State the blood parasite species.
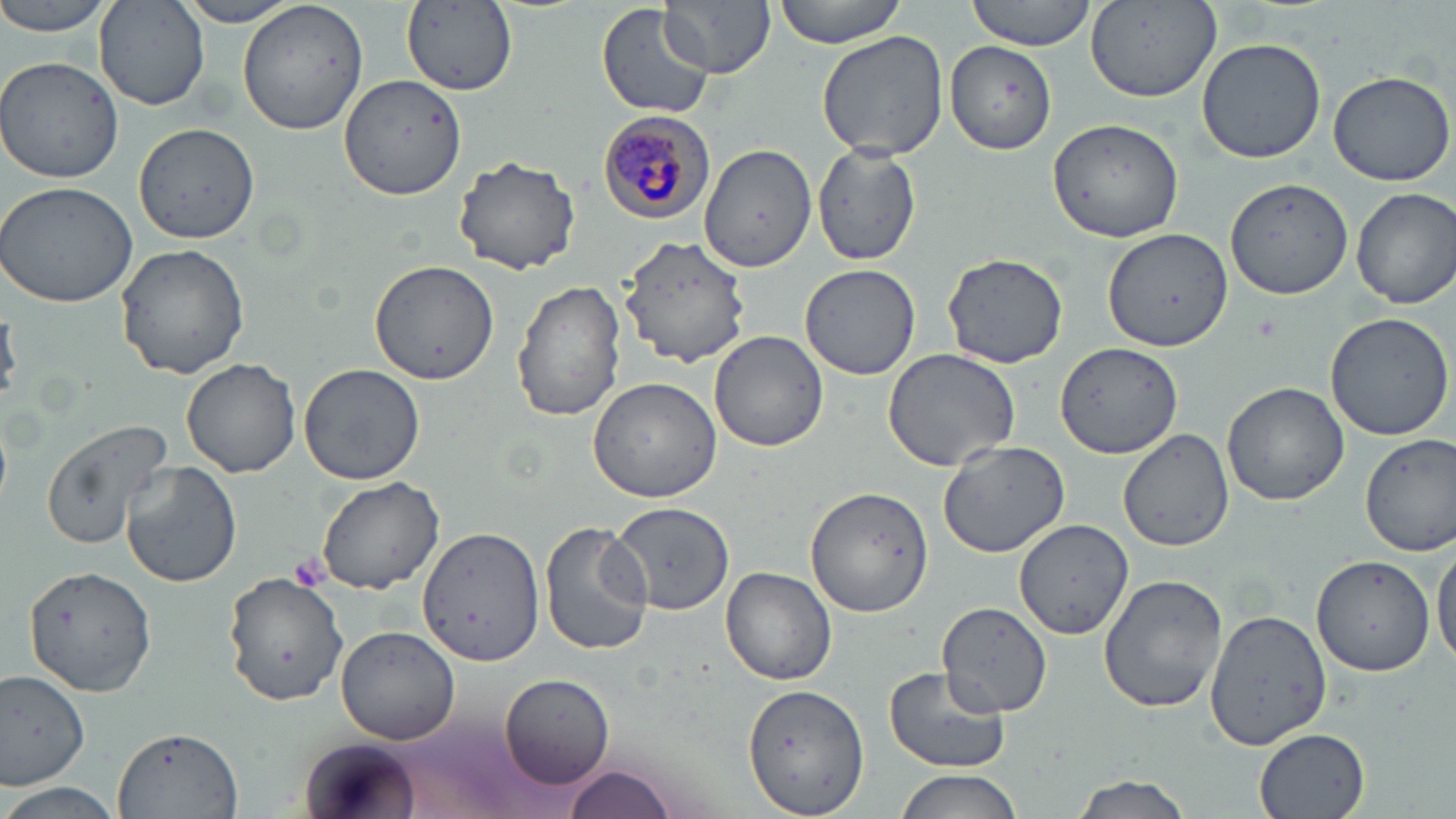
Plasmodium malariae.

preparation = thin blood film
stain = May-Grünwald-Giemsa
platelet locations = approximate bounding boxes as named x1/y1/x2/y2 corners in pixels: (x1=290, y1=553, x2=330, y2=592)
image size = 1456×819 pixels
uninfected red blood cell locations = approximate bounding boxes as named x1/y1/x2/y2 corners in pixels: (x1=0, y1=0, x2=117, y2=37), (x1=236, y1=0, x2=369, y2=135), (x1=661, y1=0, x2=775, y2=77), (x1=771, y1=0, x2=910, y2=48), (x1=964, y1=0, x2=1099, y2=51), (x1=172, y1=1, x2=305, y2=27), (x1=597, y1=1, x2=715, y2=118), (x1=1085, y1=1, x2=1224, y2=102), (x1=95, y1=2, x2=208, y2=109), (x1=402, y1=4, x2=519, y2=97), (x1=817, y1=29, x2=951, y2=160), (x1=1197, y1=37, x2=1326, y2=164), (x1=944, y1=41, x2=1056, y2=153), (x1=0, y1=57, x2=124, y2=184), (x1=1327, y1=70, x2=1456, y2=186), (x1=339, y1=74, x2=467, y2=201), (x1=1048, y1=118, x2=1184, y2=243), (x1=134, y1=121, x2=260, y2=243), (x1=700, y1=142, x2=819, y2=273), (x1=812, y1=142, x2=923, y2=265), (x1=452, y1=154, x2=580, y2=275), (x1=0, y1=180, x2=137, y2=308), (x1=1226, y1=181, x2=1352, y2=300), (x1=1352, y1=187, x2=1456, y2=309), (x1=1104, y1=227, x2=1232, y2=354), (x1=621, y1=235, x2=750, y2=366), (x1=115, y1=244, x2=249, y2=379), (x1=940, y1=250, x2=1072, y2=368), (x1=368, y1=259, x2=499, y2=387), (x1=800, y1=263, x2=921, y2=380), (x1=512, y1=279, x2=627, y2=422), (x1=1324, y1=312, x2=1456, y2=440), (x1=709, y1=330, x2=829, y2=452), (x1=1054, y1=341, x2=1188, y2=459), (x1=881, y1=347, x2=1025, y2=471), (x1=180, y1=358, x2=303, y2=477), (x1=299, y1=362, x2=426, y2=484), (x1=587, y1=374, x2=725, y2=502), (x1=1221, y1=382, x2=1349, y2=506), (x1=39, y1=419, x2=173, y2=549), (x1=1117, y1=428, x2=1236, y2=551), (x1=1360, y1=432, x2=1456, y2=555), (x1=938, y1=438, x2=1071, y2=555), (x1=120, y1=461, x2=241, y2=588), (x1=314, y1=476, x2=445, y2=594), (x1=799, y1=485, x2=935, y2=620), (x1=613, y1=503, x2=734, y2=614), (x1=1014, y1=519, x2=1137, y2=641), (x1=538, y1=521, x2=654, y2=656), (x1=419, y1=527, x2=544, y2=666), (x1=1431, y1=539, x2=1456, y2=669), (x1=1311, y1=553, x2=1440, y2=677), (x1=27, y1=566, x2=156, y2=694), (x1=720, y1=566, x2=837, y2=685), (x1=1098, y1=571, x2=1229, y2=714), (x1=225, y1=574, x2=349, y2=706), (x1=939, y1=600, x2=1054, y2=715), (x1=1202, y1=608, x2=1332, y2=752), (x1=335, y1=626, x2=460, y2=746), (x1=883, y1=665, x2=1013, y2=773), (x1=0, y1=671, x2=93, y2=789), (x1=502, y1=672, x2=615, y2=787), (x1=745, y1=681, x2=869, y2=817), (x1=1253, y1=726, x2=1373, y2=819), (x1=109, y1=727, x2=242, y2=817), (x1=299, y1=735, x2=417, y2=819), (x1=563, y1=762, x2=678, y2=819), (x1=891, y1=769, x2=1028, y2=819), (x1=1069, y1=773, x2=1195, y2=819), (x1=1, y1=781, x2=124, y2=819)
modality = light microscopy
Plasmodium malariae-infected red blood cell locations = approximate bounding boxes as named x1/y1/x2/y2 corners in pixels: (x1=598, y1=110, x2=718, y2=223)
field of view = single
magnification = 1000x